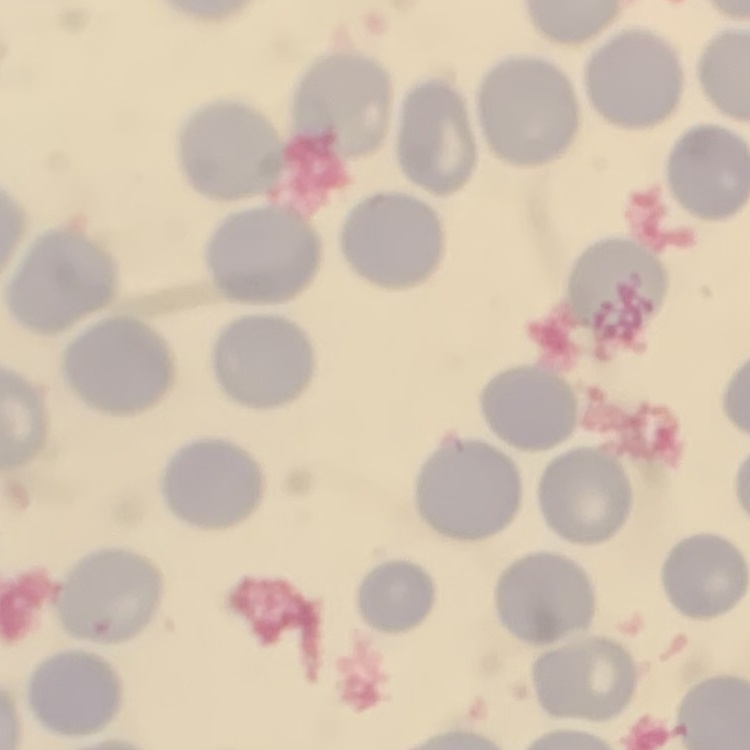

Summary:
  - Erythrocyte morphology: no rouleaux formation
  - Image type: square crop of a larger photomicrograph
  - Stain: Field's or Giemsa
  - Preparation: thin peripheral smear